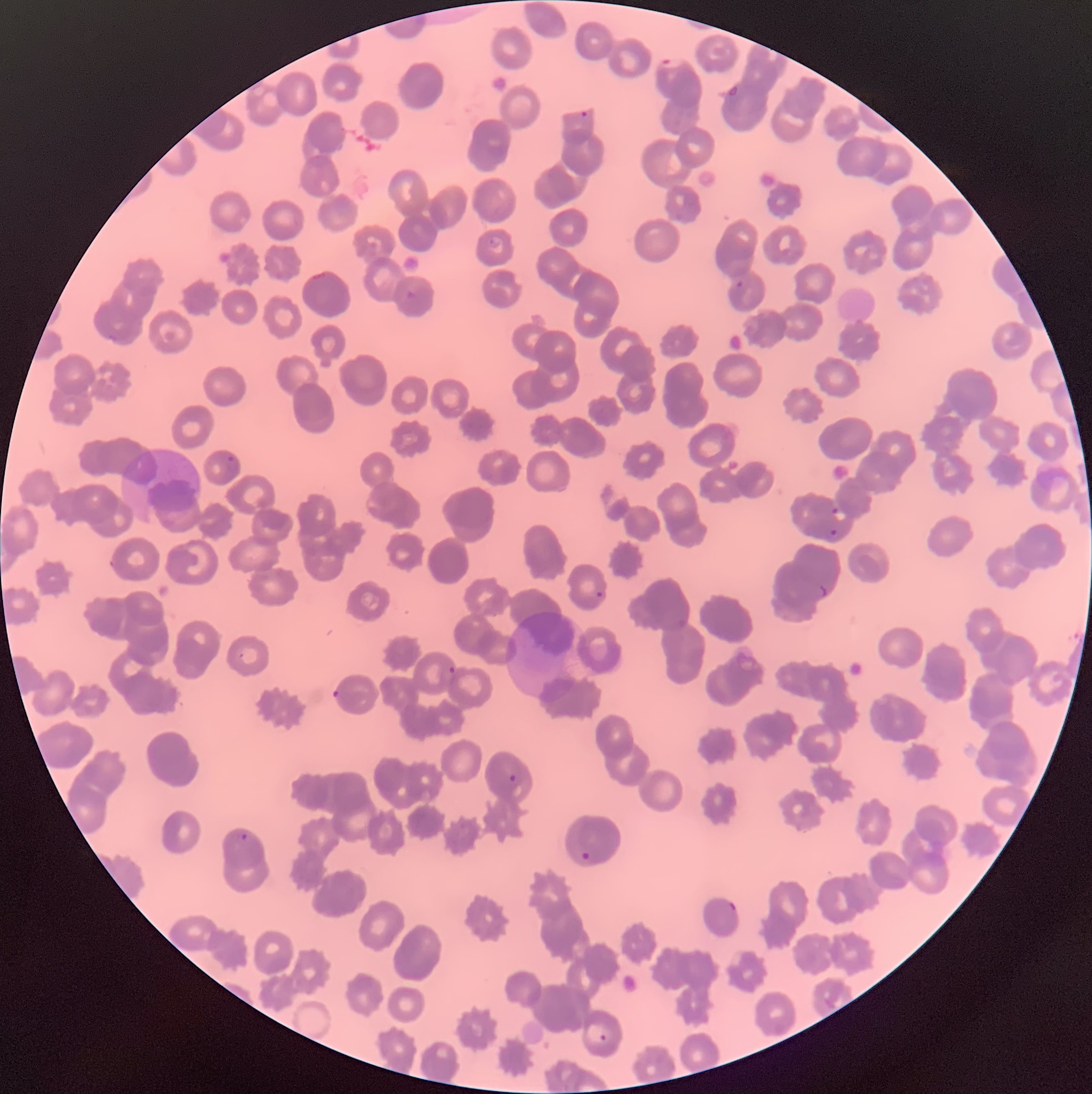
Summary:
  - Coordinate format: approximate bounding boxes as (x1, y1, x2, y2) in pixels
  - Plasmodium parasite locations: (659, 57, 683, 68), (579, 110, 588, 119), (487, 236, 503, 247), (735, 281, 743, 289), (403, 289, 417, 305), (225, 455, 239, 472), (831, 507, 847, 522), (828, 527, 840, 540), (816, 585, 828, 598), (595, 591, 604, 599), (448, 666, 456, 675), (331, 689, 341, 700), (508, 774, 517, 782), (238, 833, 249, 842), (580, 851, 591, 861), (728, 900, 737, 912), (598, 1033, 608, 1043)
  - Image size: 1092×1094 pixels
  - Preparation: thin blood smear
  - Red blood cell morphology: rouleaux formation
  - Modality: optical microscopy